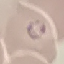

result: malaria parasites identified
stain: Giemsa
preparation: thin blood film
capture: smartphone through the microscope eyepiece
image_type: cell patch, automatically extracted from a larger field of view and resized to 64 × 64 pixels